Classify the preparation.
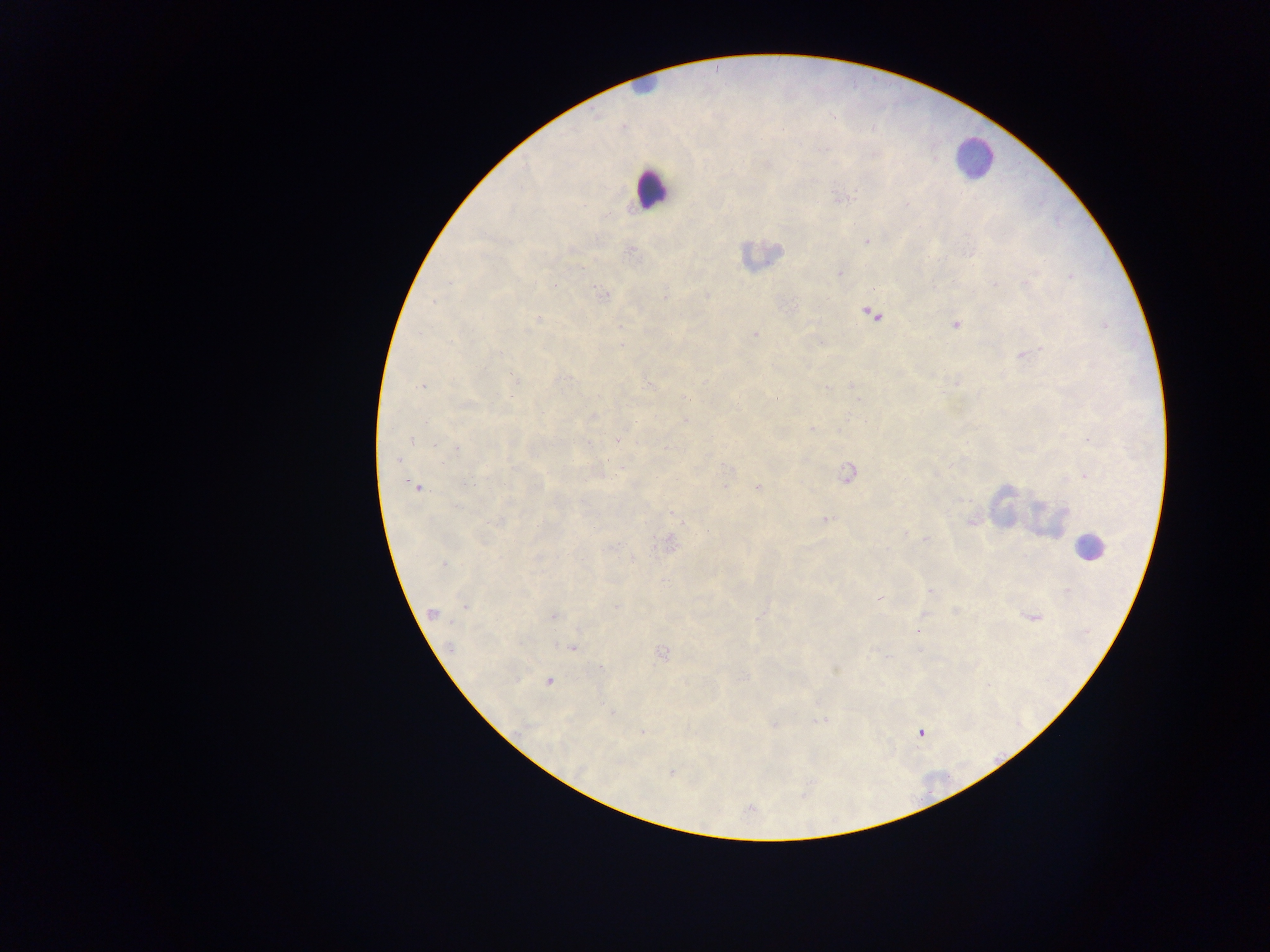

Thick blood smear.

Approximate centers as x y in pixels.
Summary:
  - Leukocyte locations: 645 84; 973 158; 651 189; 760 254; 1004 504; 1049 520; 1088 547
  - Malaria parasite locations: 842 198; 582 206; 607 215; 866 241; 631 251; 581 269; 840 274; 1070 276; 1026 283; 994 284; 602 294; 707 295; 665 298; 872 315; 538 320; 956 325; 621 326; 755 334; 1026 354; 515 379; 956 383; 852 384; 648 385; 422 386; 826 388; 684 397; 858 399; 466 404; 593 416; 686 420; 811 429; 412 440; 1092 440; 617 441; 435 445; 457 448; 396 460; 730 470; 847 474; 1085 476; 413 485; 757 486; 724 487; 582 502; 457 507; 671 513; 826 519; 971 522; 494 523; 906 534; 925 539; 669 544; 610 547; 632 558; 443 564; 931 590; 880 599; 465 606; 617 607; 955 611; 433 613; 552 616; 1033 617; 759 618; 918 631; 449 645; 571 648; 662 653; 601 668; 549 681; 612 713; 819 720; 772 725; 643 731; 921 733; 673 773; 750 809
  - Field of view: single
  - Capture: mobile-phone photograph through a microscope
  - Image size: 1270×952 pixels
  - Country: Ghana